Classify this cell by malaria status.
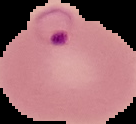
It is parasitized.

image type = segmented cell region with the area outside set to black
preparation = thin blood smear
image size = 136×124 pixels